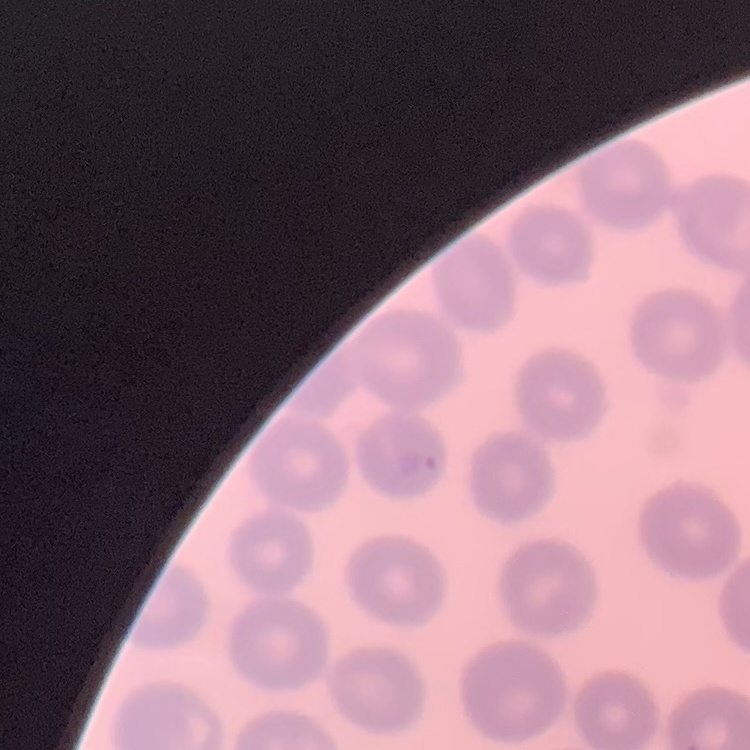 The red blood cells exhibit no rouleaux formation. Field's or Giemsa stain. Thin peripheral smear. Square crop of a larger photomicrograph.